Assess this cell for malaria.
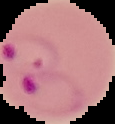
It is parasitized.

image type = cell region segmented out of the field of view; surrounding area masked to black
image size = 115×124 pixels
preparation = thin blood smear